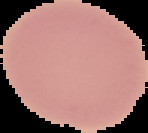

image size = 148×133 pixels
result = negative for Plasmodium parasites
image type = segmented cell region with the area outside set to black
preparation = thin blood film